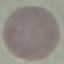

result: no malaria parasites detected
capture: smartphone camera at the microscope eyepiece
preparation: thin smear
image_type: cell patch, automatically extracted from a larger field of view and resized to 64 × 64 pixels
stain: Giemsa